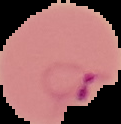
image size = 121×124 pixels
malaria status = parasitized
preparation = thin blood smear
image type = cell region segmented out of the field of view; surrounding area masked to black